Give the position of every malaria parasite and every leukocyte.
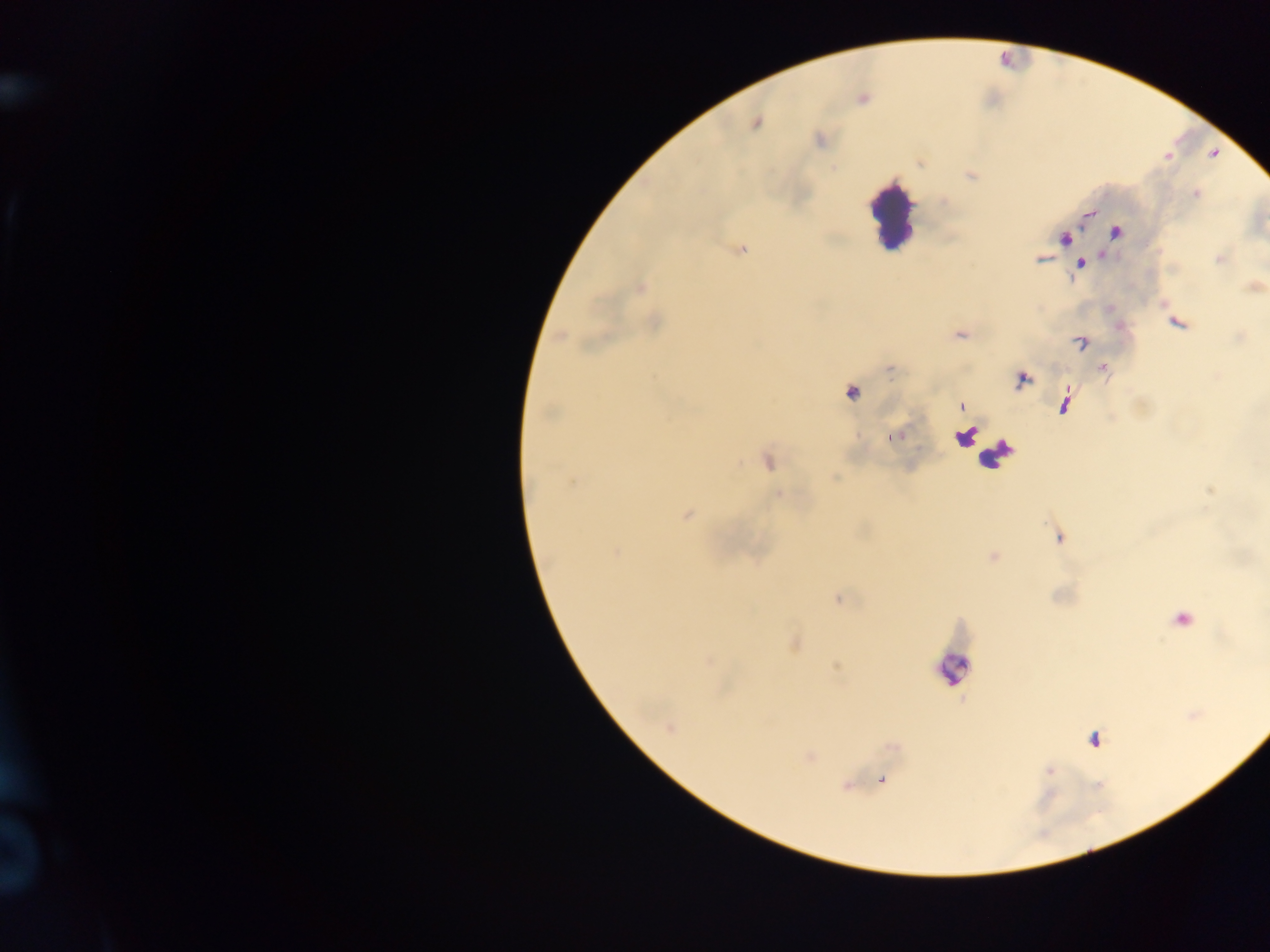

Approximate centers as (x, y) in pixels.
Malaria parasites: (756, 123), (820, 140), (834, 168), (1196, 195), (1115, 233), (1065, 239), (742, 249), (1039, 259), (1219, 259), (1081, 264), (640, 287), (654, 323), (1177, 323), (960, 334), (560, 336), (1081, 342), (1104, 371), (1023, 379), (852, 393), (1064, 403), (961, 406), (549, 413), (893, 437), (768, 462), (572, 482), (779, 495), (686, 516), (1059, 538), (616, 551), (993, 556), (1184, 619), (669, 728), (1094, 739), (1049, 770), (883, 781).
Leukocytes: (892, 217), (953, 668).

country = Ghana
field of view = single
capture = mobile-phone photograph through a microscope
image size = 1270×952 pixels
preparation = thick blood smear